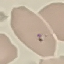 Result: no malaria parasites seen. Acquired by smartphone through the microscope eyepiece. Automatically extracted cell patch, resized to 64 × 64 pixels. Giemsa-stained preparation. Thin smear of blood.